Assess this cell for malaria.
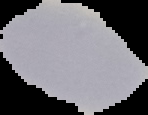

It is uninfected.

From a thin blood film. The area outside the segmented cell region is set to black. Image is 148×115 pixels.